Give the preparation type.
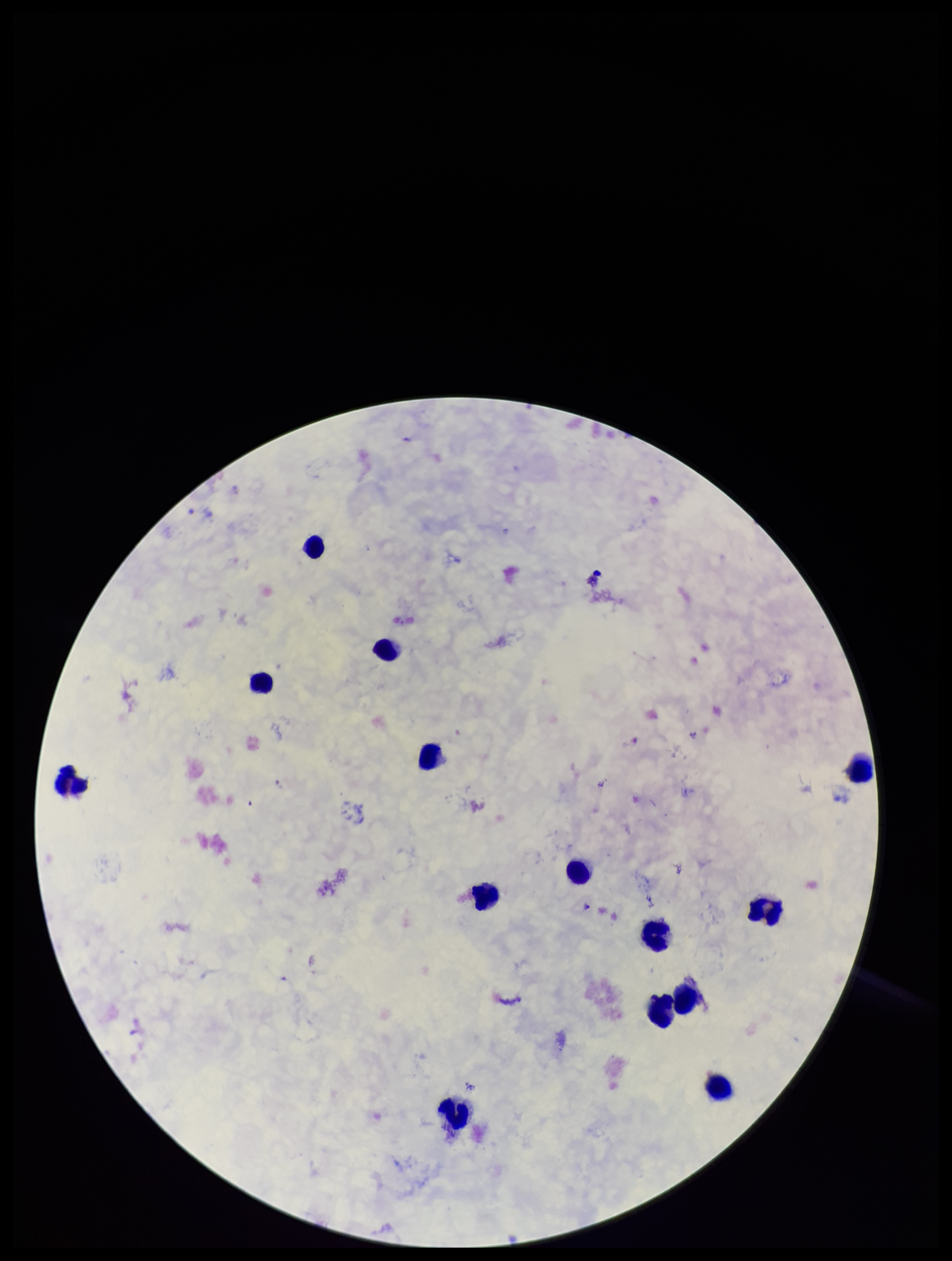

A thick smear.

Patient malaria status: infected. Leukocyte count: 14. Single field of view. Parasite count: 1. Image is 952×1261 pixels. Photographed through the microscope eyepiece with a smartphone camera. Species reported for this patient: Plasmodium falciparum. Plasmodium parasites: seen. Giemsa stain.